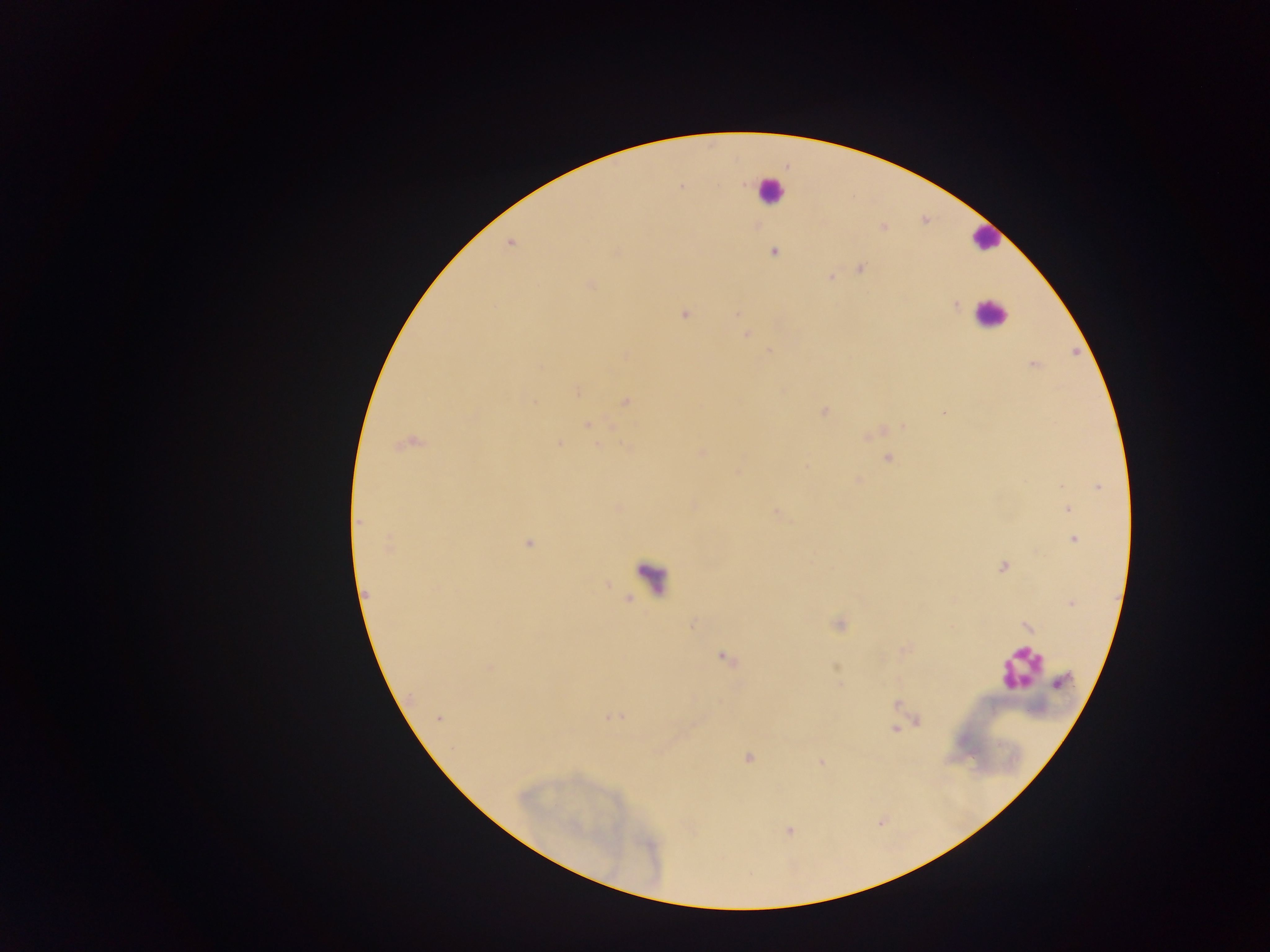
Approximate centers as {x, y} in pixels.
Summary:
  - Plasmodium parasite locations: {680, 186}, {883, 227}, {510, 242}, {615, 251}, {773, 251}, {860, 268}, {830, 277}, {590, 284}, {955, 306}, {684, 313}, {736, 314}, {747, 334}, {767, 351}, {624, 356}, {1033, 364}, {782, 390}, {577, 392}, {625, 402}, {823, 410}, {942, 413}, {587, 423}, {611, 427}, {903, 427}, {869, 434}, {408, 443}, {559, 443}, {702, 452}, {887, 457}, {806, 467}, {737, 472}, {858, 481}, {1099, 487}, {691, 504}, {1067, 509}, {775, 513}, {359, 523}, {1074, 538}, {528, 544}, {389, 546}, {1003, 566}, {607, 584}, {366, 594}, {629, 598}, {1071, 602}, {694, 623}, {839, 624}, {1026, 626}, {725, 659}, {488, 666}, {1061, 682}, {897, 705}, {614, 716}, {438, 718}, {917, 720}, {894, 727}, {748, 757}, {821, 762}, {880, 821}, {788, 831}
  - Leukocyte locations: {770, 189}, {985, 238}, {990, 314}, {653, 578}, {1021, 667}
  - Image size: 1270×952 pixels
  - Field of view: single
  - Capture: mobile-phone photograph through a microscope
  - Preparation: thick blood smear
  - Country: Ghana